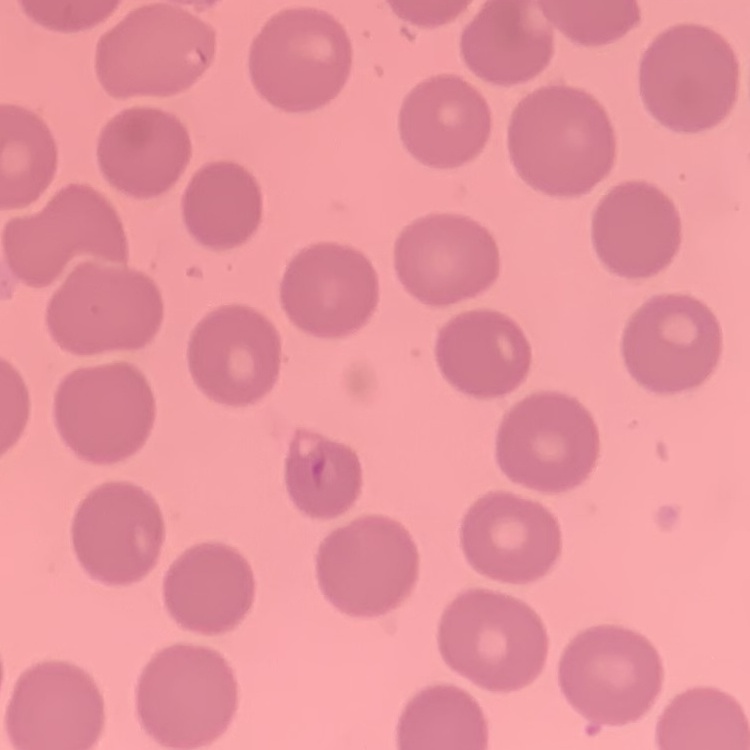

erythrocyte morphology = no rouleaux formation
stain = Field's or Giemsa
preparation = thin blood film
image type = one tile cut from a larger photomicrograph